Point out leukocytes.
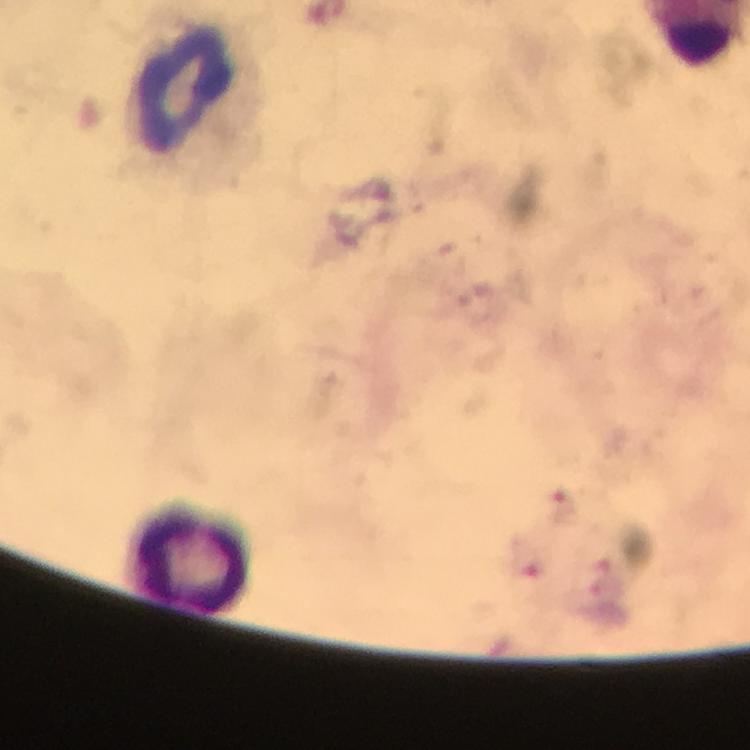

Approximate centers as [x, y] in pixels.
Leukocytes: [188, 85], [193, 555].

Summary:
  - Preparation: thick smear
  - Capture: smartphone mounted on the microscope
  - Immersion oil: applied
  - Plasmodium parasites: none detected
  - Context: from a malaria diagnostic workup
  - Magnification: 100x
  - Image size: 750×750 pixels
  - Stain: Giemsa
  - Cropped from: a single field of view